State which cell type is depicted.
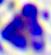
This is a leukocyte.

{
  "magnification": "400x",
  "modality": "photomicrograph"
}